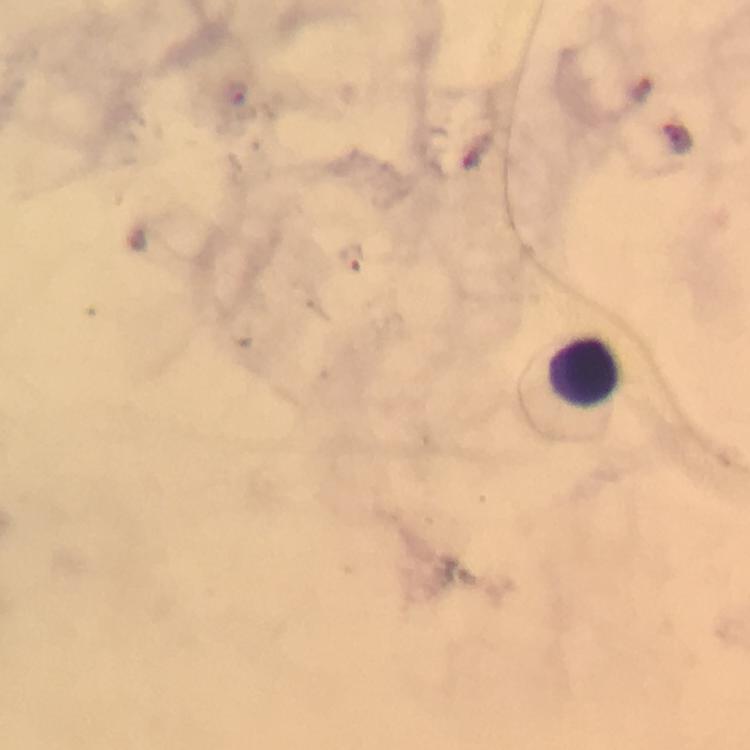
Plasmodium parasite locations = approximate centers as {x, y} in pixels: {237, 93}, {352, 256}
capture = smartphone photograph through a microscope
preparation = thick smear
magnification = 100x
cropped from = one field of view
context = from a diagnostic examination for malaria
stain = Giemsa
image size = 750×750 pixels
leukocyte locations = approximate centers as {x, y} in pixels: {586, 372}
immersion oil = applied